Classify this cell by malaria status.
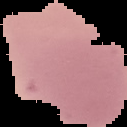
It is uninfected.

Summary:
  - Image type: segmented cell region on a black background
  - Image size: 127×127 pixels
  - Preparation: thin blood film